Report the malaria status of this cell.
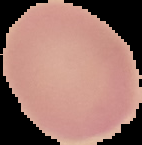

It is uninfected.

preparation: thin blood film
image_size: 142×145 pixels
image_type: segmented cell region with the area outside set to black